Report the malaria status of this cell.
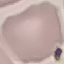
It is uninfected.

{
  "image_type": "automatically extracted cell patch, resized to 64 × 64 pixels",
  "stain": "Giemsa",
  "capture": "smartphone camera at the microscope eyepiece",
  "preparation": "thin blood smear"
}